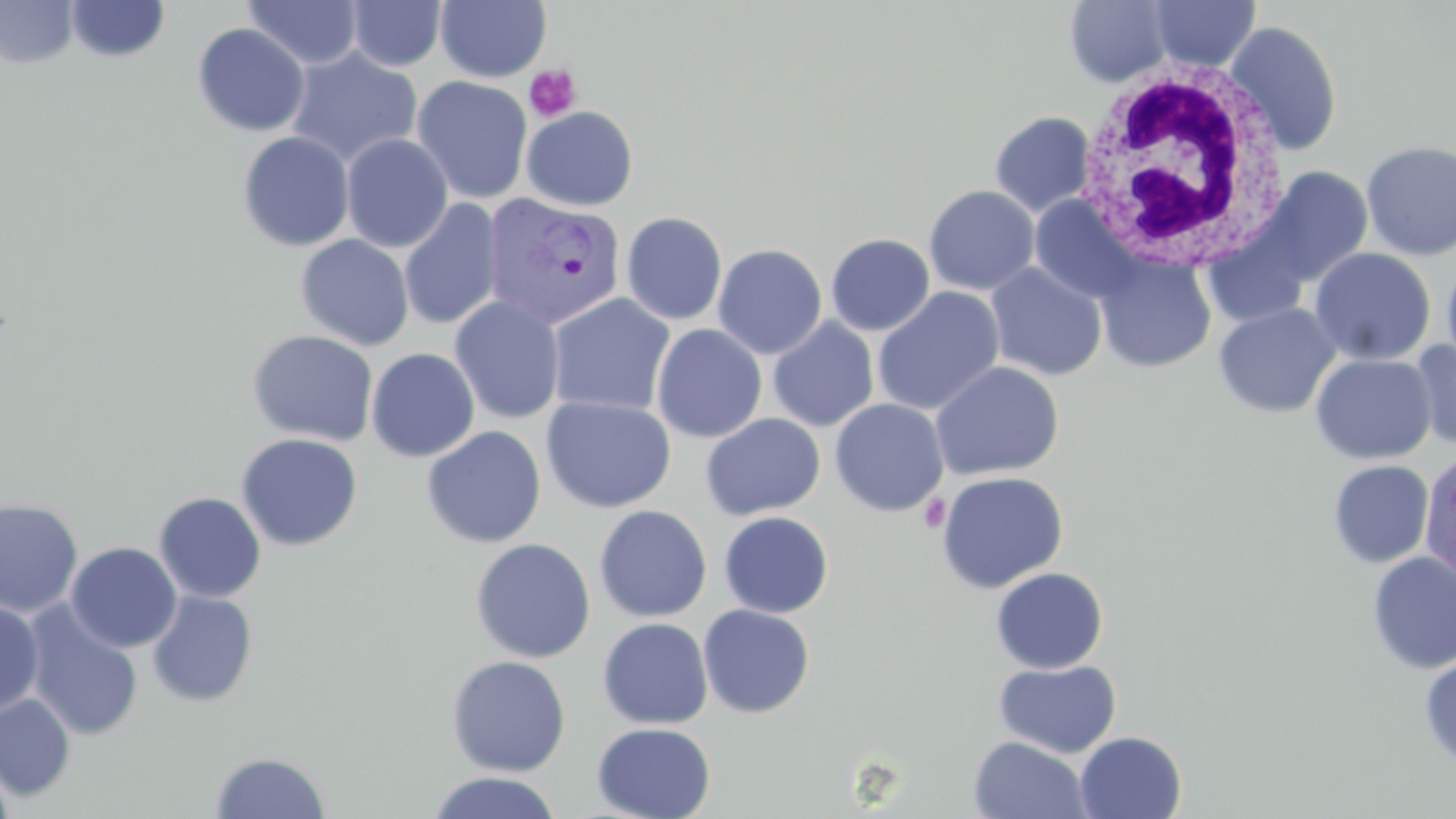

slide_level_diagnosis: Plasmodium vivax
magnification: 1000x
plasmodium_vivax_infected_red_blood_cell_locations: 'approximate bounding boxes as (x1, y1, x2, y2) in pixels: (481, 192, 627, 330)'
field_of_view: one of a larger specimen
modality: optical microscopy
stain: May-Grünwald-Giemsa
white_blood_cell_locations: 'approximate bounding boxes as (x1, y1, x2, y2) in pixels: (1073, 64, 1291, 273)'
platelet_locations: 'approximate bounding boxes as (x1, y1, x2, y2) in pixels: (524, 64, 581, 122), (918, 494, 951, 533)'
preparation: thin blood film
uninfected_red_blood_cell_locations: 'approximate bounding boxes as (x1, y1, x2, y2) in pixels: (65, 0, 171, 63), (244, 0, 364, 69), (435, 0, 551, 83), (1146, 0, 1261, 72), (0, 1, 79, 68), (346, 1, 446, 71), (1064, 1, 1176, 87), (1224, 20, 1343, 156), (192, 23, 310, 137), (285, 48, 422, 169), (412, 76, 533, 204), (521, 106, 638, 211), (989, 111, 1096, 216), (237, 131, 355, 251), (341, 133, 453, 252), (1360, 139, 1456, 261), (1252, 166, 1372, 290), (923, 185, 1040, 296), (1028, 195, 1142, 305), (399, 198, 503, 331), (622, 211, 728, 325), (825, 233, 935, 336), (296, 234, 414, 351), (713, 243, 827, 359), (1308, 247, 1436, 365), (1093, 249, 1216, 373), (1441, 254, 1456, 376), (985, 261, 1108, 381), (872, 287, 1005, 416), (547, 293, 675, 417), (449, 296, 565, 424), (1213, 303, 1341, 418), (768, 318, 879, 432), (651, 323, 767, 443), (246, 329, 378, 446), (1409, 339, 1456, 452), (366, 347, 480, 462), (1310, 353, 1436, 464), (930, 361, 1064, 480), (540, 395, 676, 513), (829, 398, 949, 516), (701, 413, 825, 520), (422, 426, 546, 548), (237, 433, 363, 551), (1418, 451, 1456, 586), (1328, 460, 1434, 568), (936, 471, 1069, 592), (153, 492, 266, 602), (0, 498, 83, 619), (593, 505, 712, 622), (718, 511, 833, 618), (470, 538, 595, 663), (65, 542, 182, 652), (1367, 552, 1456, 673), (990, 567, 1109, 673), (147, 589, 258, 708), (0, 599, 44, 715), (22, 601, 144, 741), (698, 604, 815, 718), (597, 617, 713, 729), (1419, 654, 1456, 770), (446, 655, 571, 776), (994, 659, 1121, 758), (0, 693, 76, 800), (592, 722, 716, 819), (1075, 731, 1187, 818), (968, 735, 1093, 818), (210, 750, 331, 818), (0, 757, 15, 819), (426, 771, 562, 819)'
image_size: 1456×819 pixels